Report the malaria status of this cell.
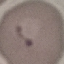

It is parasitized.

Giemsa-stained preparation. Thin blood film. Cell patch, automatically extracted from a larger field of view and resized to 64 × 64 pixels. Acquired by smartphone through the microscope eyepiece.